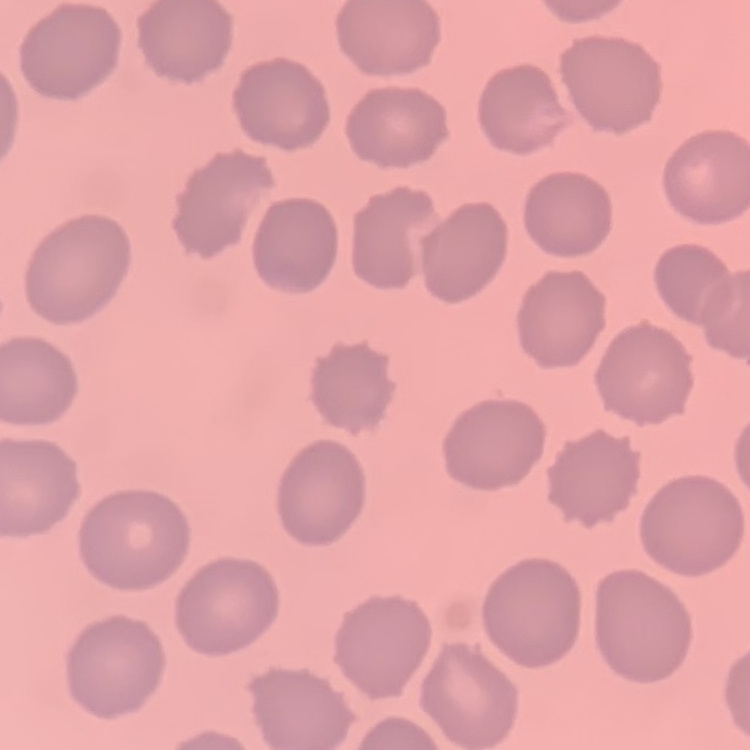
red blood cell morphology = no rouleaux formation
image type = square crop of a larger photomicrograph
stain = Field's or Giemsa
preparation = thin peripheral smear